Name the blood parasite species.
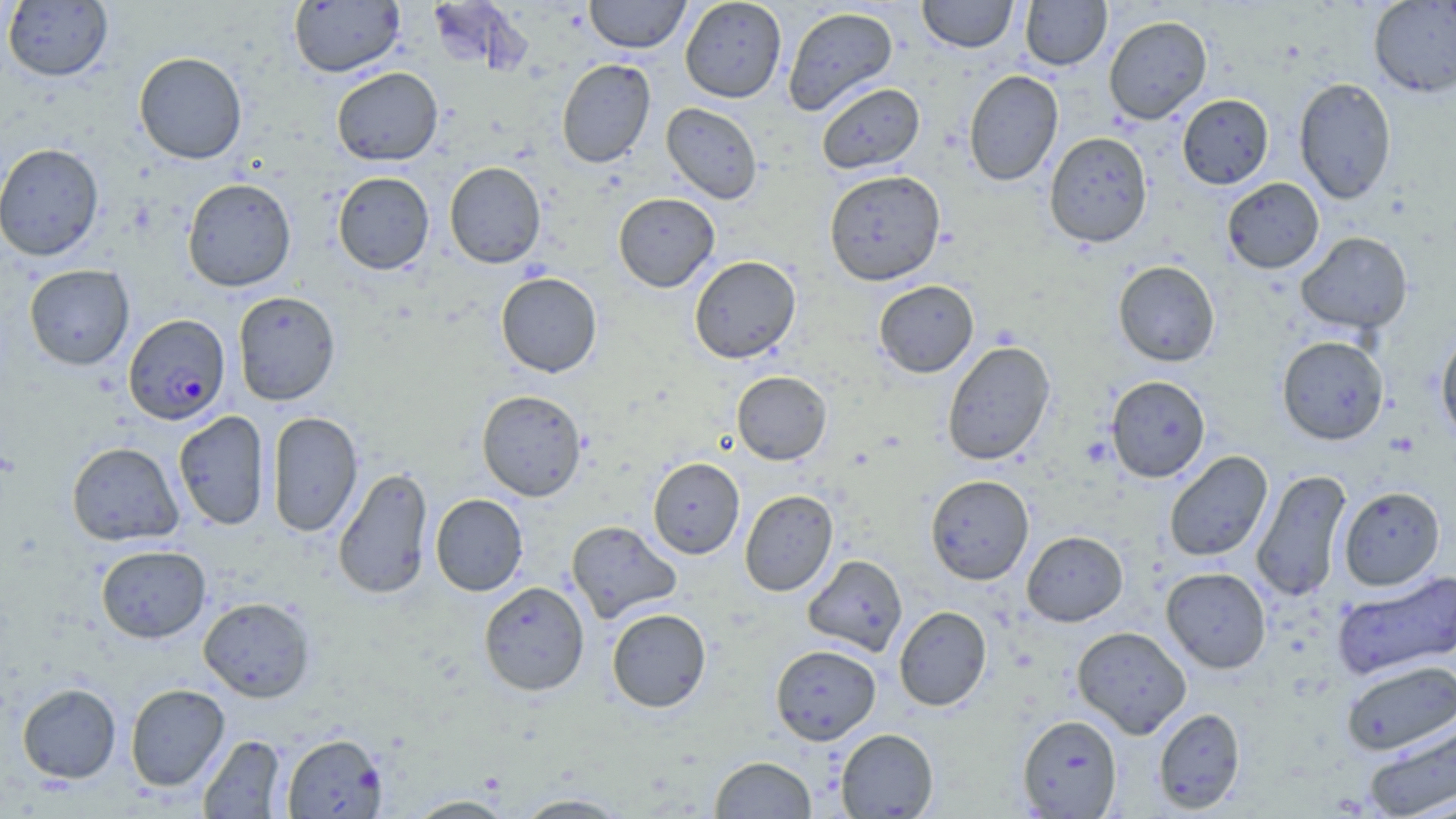

Plasmodium falciparum.

Approximate bounding boxes as (x1, y1, x2, y2) in pixels. Uninfected red blood cell locations: (584, 0, 690, 53), (680, 0, 787, 103), (917, 0, 1018, 52), (1020, 0, 1111, 70), (3, 1, 113, 81), (288, 1, 404, 77), (1368, 1, 1456, 97), (425, 2, 527, 72), (782, 6, 898, 116), (1103, 15, 1212, 124), (134, 51, 247, 164), (556, 59, 656, 168), (331, 67, 443, 166), (963, 69, 1064, 187), (1294, 77, 1396, 204), (816, 82, 925, 174), (1177, 94, 1274, 189), (661, 103, 763, 204), (1044, 131, 1153, 248), (0, 142, 104, 261), (444, 161, 546, 268), (824, 169, 946, 286), (333, 172, 434, 275), (182, 177, 297, 291), (1222, 178, 1324, 274), (613, 192, 720, 292), (1296, 231, 1413, 334), (689, 255, 801, 364), (1113, 260, 1220, 367), (24, 264, 134, 370), (495, 272, 602, 377), (873, 280, 978, 377), (233, 290, 341, 405), (1435, 326, 1456, 445), (1276, 336, 1389, 445), (941, 341, 1055, 466), (731, 371, 832, 465), (1105, 375, 1211, 482), (476, 389, 587, 501), (173, 410, 270, 530), (267, 411, 363, 538), (66, 441, 183, 546), (1164, 451, 1273, 562), (648, 457, 744, 559), (333, 467, 434, 600), (1251, 469, 1352, 602), (925, 475, 1034, 585), (1339, 486, 1445, 590), (739, 490, 838, 596), (430, 493, 528, 596), (566, 520, 682, 623), (1022, 531, 1127, 626), (95, 544, 211, 643), (802, 554, 907, 656), (1161, 567, 1271, 673), (1332, 570, 1456, 681), (478, 581, 590, 696), (198, 596, 316, 702), (894, 606, 992, 711), (607, 608, 711, 712), (1072, 626, 1192, 738), (770, 644, 881, 745), (1341, 659, 1455, 756), (17, 683, 121, 783), (125, 683, 229, 791), (1153, 708, 1245, 814), (1017, 714, 1122, 817), (1362, 716, 1455, 819), (835, 728, 939, 818), (281, 733, 388, 818), (198, 734, 286, 818), (709, 756, 816, 818), (511, 793, 632, 818), (403, 794, 517, 818). Plasmodium falciparum-infected red blood cell locations: (123, 314, 230, 425). May-Grünwald-Giemsa-stained preparation. One field of a larger specimen. Image is 1456×819 pixels. Optical microscopy. 1000x magnification. Thin blood smear.